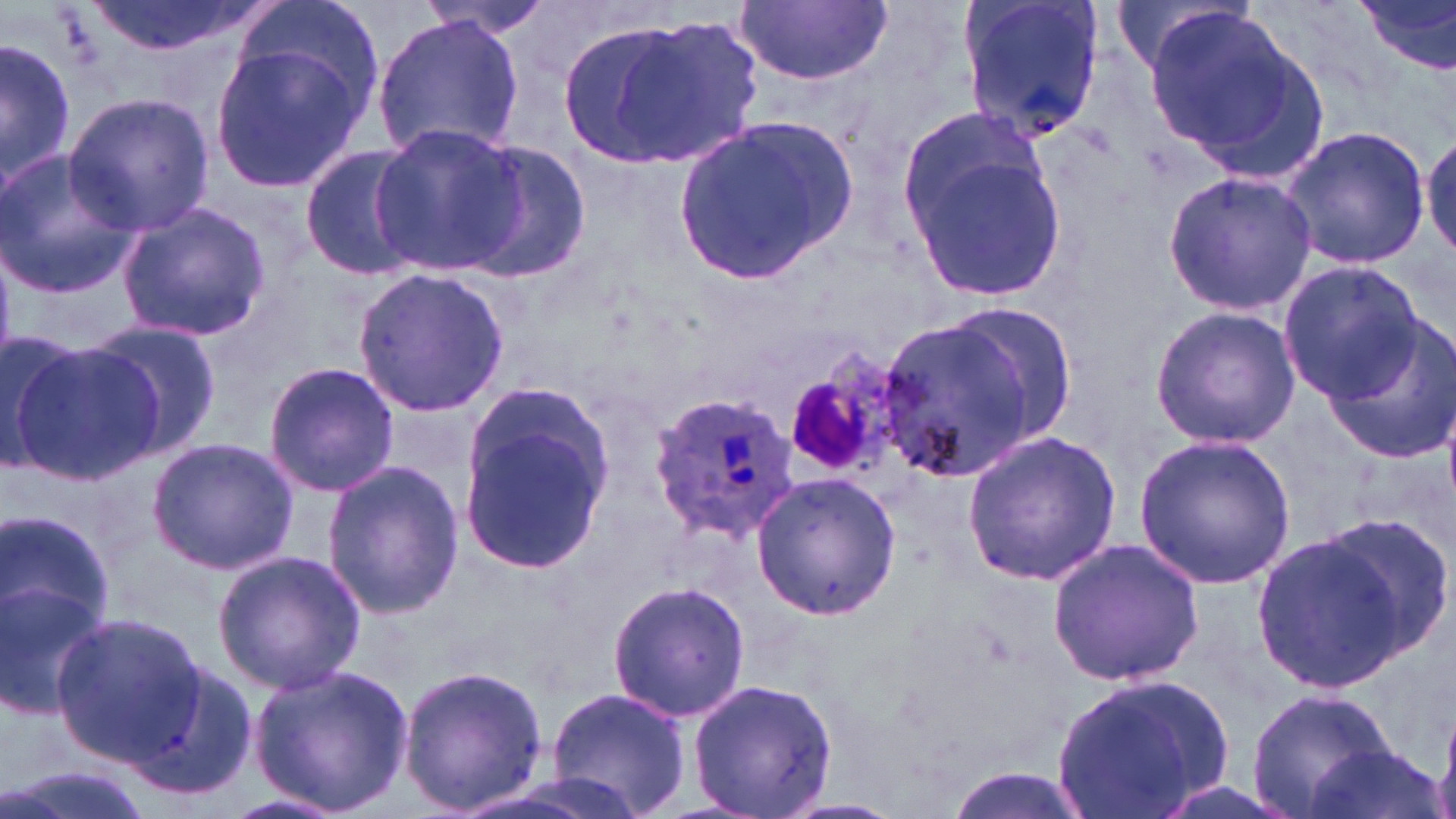
Summary:
  - Coordinate format: approximate bounding boxes as (x1,y1)-(x2,y2) corner pairs in pixels
  - Plasmodium ovale-infected red blood cell locations: (649,392)-(799,538)
  - Uninfected red blood cell locations: (80,0)-(262,58), (228,0)-(384,128), (416,0)-(559,39), (958,0)-(1106,144), (1352,0)-(1456,83), (734,1)-(893,86), (1138,2)-(1302,158), (370,11)-(524,161), (587,14)-(765,170), (1,34)-(74,190), (206,39)-(371,191), (62,94)-(213,234), (894,109)-(1066,304), (670,112)-(857,288), (368,120)-(524,275), (1279,124)-(1431,271), (1420,132)-(1456,262), (458,138)-(592,283), (298,143)-(425,281), (0,149)-(141,295), (1163,169)-(1318,315), (115,202)-(271,341), (1278,260)-(1425,401), (350,265)-(511,417), (940,305)-(1079,436), (1149,305)-(1300,449), (1320,314)-(1456,466), (881,317)-(1038,477), (80,319)-(225,463), (0,329)-(88,470), (7,337)-(158,485), (262,361)-(400,498), (457,380)-(618,576), (961,430)-(1123,587), (1134,434)-(1296,588), (146,438)-(301,574), (321,460)-(466,618), (751,471)-(902,621), (3,501)-(117,682), (1321,512)-(1455,659), (1249,526)-(1416,691), (1047,535)-(1206,688), (211,550)-(366,695), (0,580)-(109,717), (607,580)-(751,723), (51,613)-(205,767), (123,659)-(256,801), (247,662)-(416,815), (398,663)-(549,815), (1052,669)-(1239,819), (687,675)-(838,819), (1245,685)-(1394,819), (545,686)-(694,819), (1301,742)-(1445,819), (1,762)-(155,819), (216,792)-(348,819)
  - Platelet locations: (789,376)-(879,472)
  - Slide-level diagnosis: Plasmodium ovale
  - Stain: May-Grünwald-Giemsa
  - Image size: 1456×819 pixels
  - Preparation: thin blood film
  - Modality: optical microscopy
  - Magnification: 1000x
  - Field of view: single